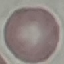
Malaria status: uninfected. Automatically extracted cell patch, resized to 64 × 64 pixels. Thin blood film. Acquired by smartphone through the microscope eyepiece. Giemsa-stained preparation.